Outline each blood parasite and name the species.
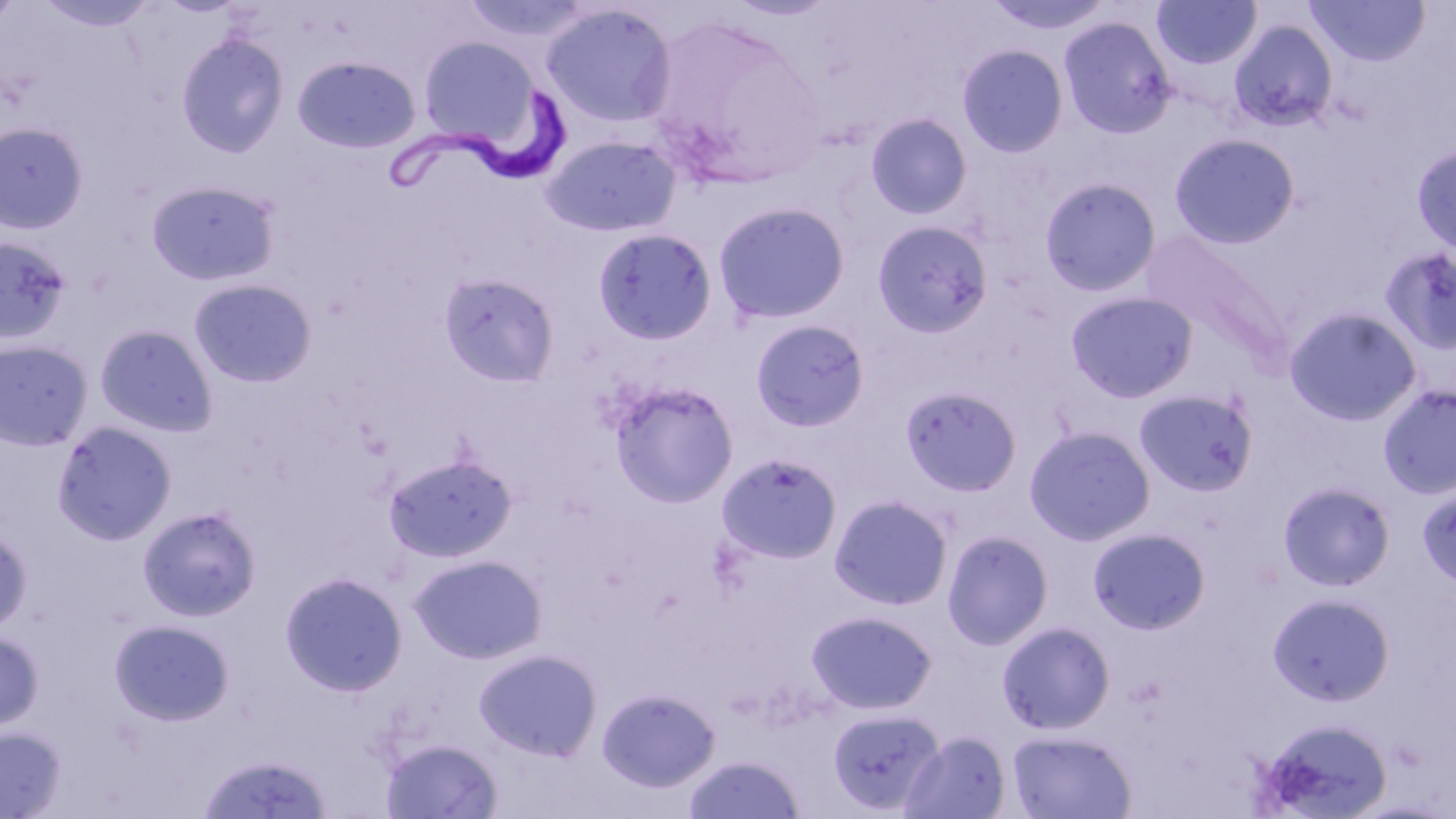

Approximate bounding boxes as [x1, y1, x2, y2] in pixels.
Trypanosoma brucei: [381, 85, 574, 203].
No Plasmodium falciparum, Plasmodium ovale, Plasmodium malariae, Plasmodium vivax, or Babesia divergens observed.

Summary:
  - Uninfected red blood cell locations: [0, 0, 24, 28], [34, 0, 160, 32], [983, 0, 1116, 35], [1151, 0, 1262, 70], [1306, 0, 1430, 66], [541, 3, 677, 129], [640, 13, 831, 189], [1057, 14, 1178, 139], [1229, 20, 1339, 133], [176, 32, 290, 159], [418, 35, 541, 148], [957, 43, 1069, 158], [293, 55, 421, 153], [865, 112, 973, 220], [0, 122, 88, 235], [1169, 133, 1300, 249], [540, 134, 682, 238], [1412, 143, 1456, 255], [146, 178, 281, 286], [1039, 178, 1161, 296], [713, 200, 851, 325], [871, 219, 994, 337], [592, 227, 718, 345], [1141, 230, 1291, 361], [0, 236, 72, 344], [1379, 245, 1456, 355], [439, 271, 561, 388], [189, 278, 317, 388], [1065, 291, 1198, 403], [1284, 306, 1423, 426], [750, 319, 871, 433], [95, 324, 219, 437], [0, 338, 94, 452], [608, 379, 740, 508], [1377, 383, 1456, 500], [900, 385, 1022, 497], [1135, 389, 1259, 496], [51, 421, 178, 545], [1024, 425, 1157, 546], [382, 451, 518, 564], [716, 452, 843, 565], [1277, 481, 1396, 592], [1417, 485, 1456, 593], [829, 494, 954, 611], [137, 506, 262, 622], [0, 526, 33, 635], [1087, 527, 1211, 634], [942, 530, 1054, 649], [410, 553, 546, 664], [279, 571, 408, 696], [1267, 592, 1395, 706], [806, 610, 938, 715], [109, 618, 235, 726], [997, 621, 1115, 734], [0, 631, 44, 732], [474, 648, 603, 761], [597, 687, 720, 792], [827, 707, 944, 814], [1254, 716, 1393, 819], [0, 726, 67, 818], [1007, 729, 1137, 819], [902, 730, 1011, 818], [380, 737, 503, 818], [196, 751, 334, 818], [682, 754, 807, 819]
  - Slide-level diagnosis: Trypanosoma brucei
  - Image size: 1456×819 pixels
  - Preparation: thin blood smear
  - Field of view: one of a larger specimen
  - Magnification: 1000x
  - Stain: May-Grünwald-Giemsa
  - Modality: optical microscopy